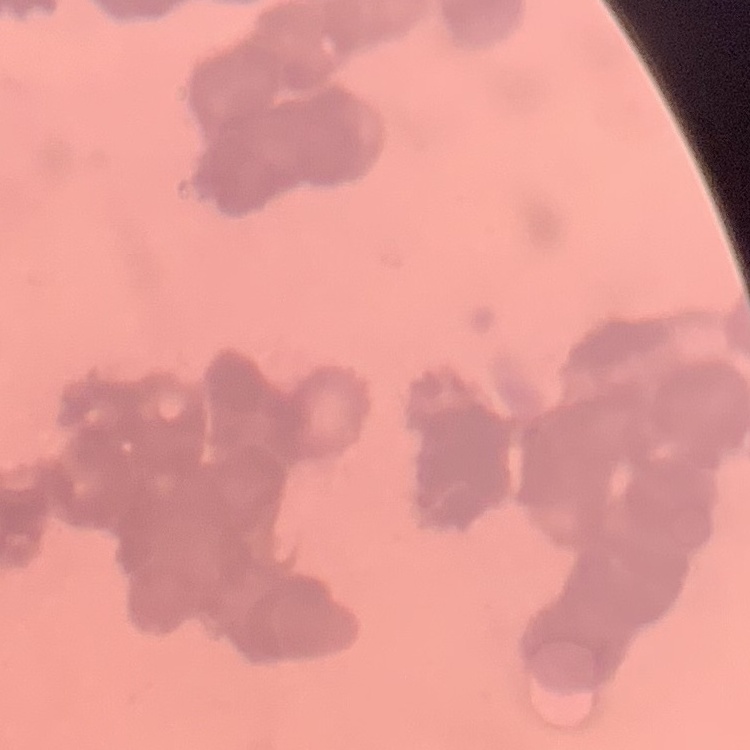

erythrocyte morphology = rouleaux formation
preparation = thin peripheral smear
stain = Field's or Giemsa
image type = one tile cut from a larger photomicrograph